Name the parasite shown.
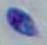

This is Toxoplasma gondii.

magnification = 1000x
modality = micrograph